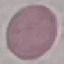 Result: no malaria parasites detected. Thin blood smear. Photographed with a smartphone camera at the microscope eyepiece. Cell patch, automatically extracted from a larger field of view and resized to 64 × 64 pixels. Giemsa-stained preparation.